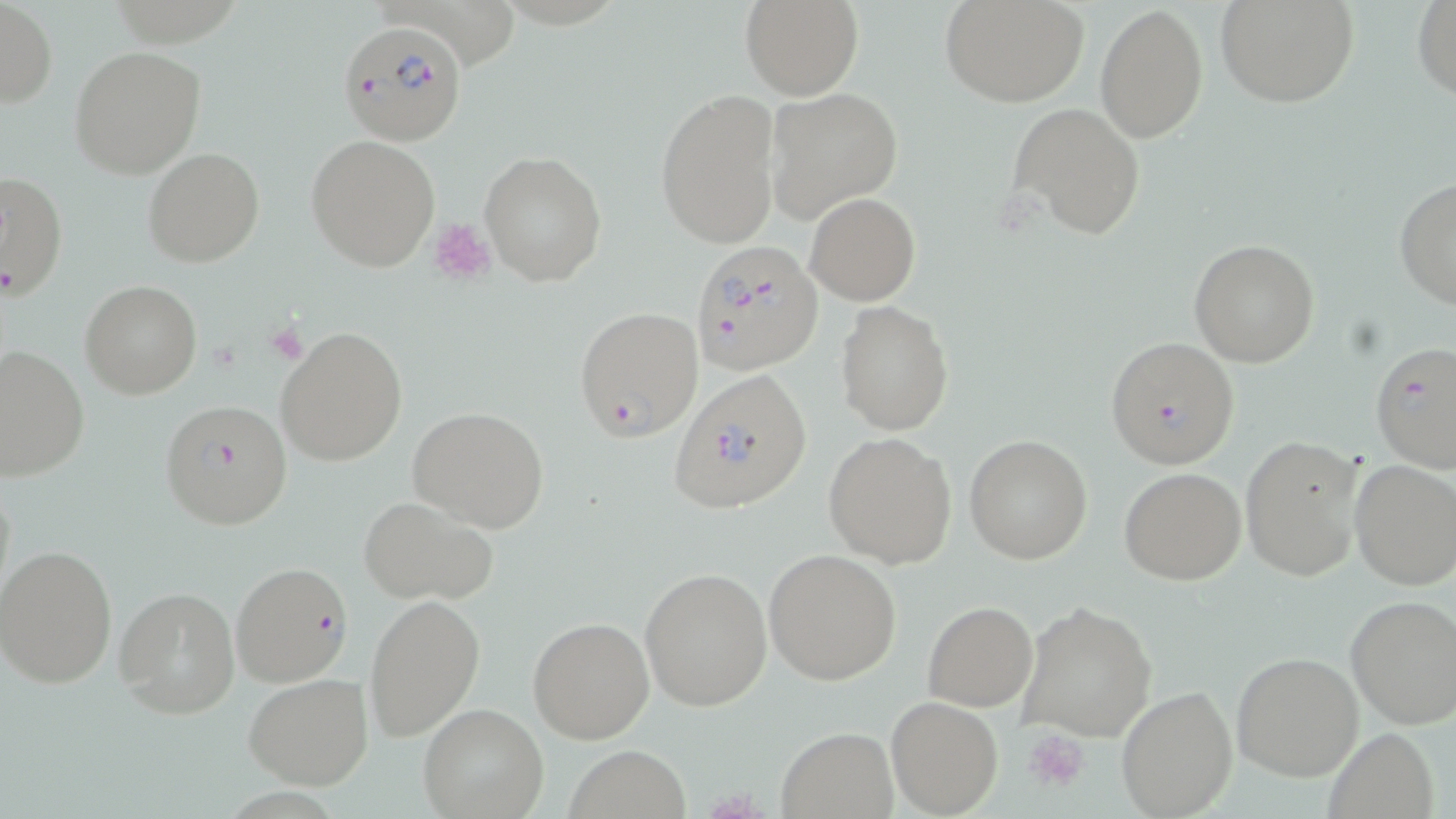
Summary:
  - Coordinate format: approximate bounding boxes as [x1, y1, x2, y2] in pixels
  - Platelet locations: [428, 217, 497, 285], [1025, 728, 1090, 792]
  - Uninfected red blood cell locations: [740, 0, 863, 101], [940, 0, 1089, 108], [1217, 0, 1360, 108], [1411, 0, 1456, 102], [0, 1, 59, 108], [1096, 3, 1209, 143], [69, 45, 206, 179], [765, 86, 903, 222], [654, 88, 783, 250], [1009, 104, 1146, 239], [306, 135, 440, 271], [142, 147, 265, 267], [478, 151, 607, 288], [0, 172, 68, 301], [1393, 175, 1456, 311], [805, 192, 921, 306], [1189, 238, 1320, 368], [80, 281, 202, 400], [836, 300, 955, 436], [275, 324, 407, 467], [0, 345, 90, 481], [407, 405, 552, 533], [823, 433, 957, 568], [964, 434, 1093, 564], [1239, 435, 1366, 584], [1348, 458, 1456, 591], [1120, 467, 1247, 585], [355, 494, 501, 605], [1, 545, 120, 689], [763, 548, 902, 686], [640, 566, 771, 709], [115, 586, 240, 719], [362, 593, 487, 743], [1344, 596, 1456, 731], [1016, 600, 1158, 743], [922, 601, 1037, 711], [528, 615, 654, 742], [1231, 651, 1364, 780], [243, 674, 372, 790], [1116, 685, 1238, 818], [886, 696, 1003, 817], [417, 703, 548, 819], [1321, 727, 1440, 818], [775, 728, 899, 816], [566, 745, 692, 818]
  - Plasmodium falciparum-infected red blood cell locations: [339, 17, 468, 144], [688, 240, 823, 376], [574, 306, 704, 442], [1104, 336, 1240, 469], [1369, 341, 1456, 473], [668, 368, 813, 516], [158, 399, 294, 529], [229, 560, 354, 687]
  - Slide-level diagnosis: Plasmodium falciparum
  - Modality: light microscopy
  - Field of view: single
  - Stain: May-Grünwald-Giemsa
  - Preparation: thin blood smear
  - Magnification: 1000x
  - Image size: 1456×819 pixels